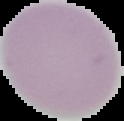

Result: negative for malaria parasites. Segmented cell region on a black background. From a thin blood film. Image is 124×121 pixels.